Outline each blood parasite and name the species.
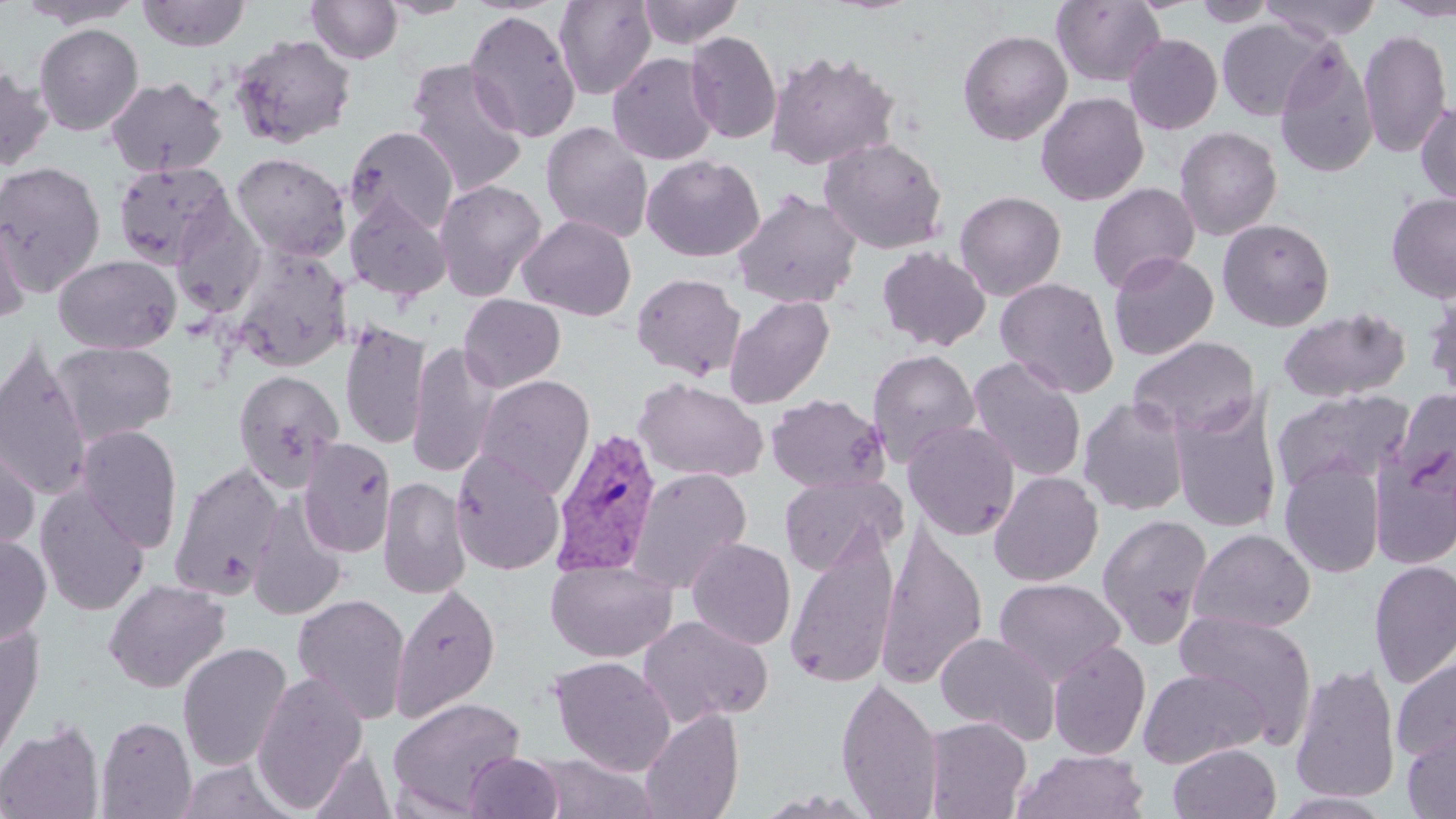
Approximate bounding boxes as named x1/y1/x2/y2 corners in pixels.
Plasmodium vivax-infected red blood cells: (x1=550, y1=426, x2=663, y2=578).
No Plasmodium falciparum, Plasmodium ovale, Plasmodium malariae, Babesia divergens, or Trypanosoma brucei observed.

slide-level diagnosis = Plasmodium vivax
modality = optical microscopy
field of view = single
stain = May-Grünwald-Giemsa
uninfected red blood cell locations = approximate bounding boxes as named x1/y1/x2/y2 corners in pixels: (x1=14, y1=0, x2=145, y2=28), (x1=136, y1=0, x2=251, y2=51), (x1=305, y1=0, x2=404, y2=65), (x1=378, y1=0, x2=476, y2=19), (x1=553, y1=0, x2=657, y2=100), (x1=636, y1=0, x2=744, y2=48), (x1=1051, y1=0, x2=1166, y2=87), (x1=1191, y1=0, x2=1279, y2=27), (x1=1259, y1=0, x2=1384, y2=43), (x1=1384, y1=0, x2=1456, y2=21), (x1=463, y1=9, x2=581, y2=143), (x1=1217, y1=18, x2=1329, y2=122), (x1=34, y1=23, x2=144, y2=135), (x1=1359, y1=28, x2=1451, y2=159), (x1=957, y1=29, x2=1072, y2=145), (x1=685, y1=30, x2=782, y2=144), (x1=1123, y1=33, x2=1223, y2=134), (x1=229, y1=34, x2=357, y2=149), (x1=1274, y1=41, x2=1378, y2=180), (x1=765, y1=49, x2=900, y2=170), (x1=606, y1=52, x2=719, y2=165), (x1=405, y1=59, x2=528, y2=197), (x1=0, y1=64, x2=55, y2=171), (x1=105, y1=76, x2=227, y2=177), (x1=1035, y1=91, x2=1149, y2=206), (x1=1416, y1=97, x2=1456, y2=205), (x1=541, y1=122, x2=654, y2=244), (x1=344, y1=126, x2=459, y2=235), (x1=1174, y1=126, x2=1282, y2=241), (x1=819, y1=136, x2=949, y2=254), (x1=231, y1=151, x2=351, y2=261), (x1=641, y1=154, x2=765, y2=262), (x1=0, y1=161, x2=106, y2=294), (x1=112, y1=161, x2=235, y2=269), (x1=433, y1=178, x2=548, y2=300), (x1=1087, y1=182, x2=1200, y2=293), (x1=732, y1=189, x2=862, y2=309), (x1=954, y1=190, x2=1067, y2=300), (x1=1386, y1=190, x2=1456, y2=303), (x1=344, y1=194, x2=453, y2=300), (x1=170, y1=207, x2=265, y2=316), (x1=0, y1=210, x2=30, y2=325), (x1=517, y1=214, x2=637, y2=321), (x1=1217, y1=218, x2=1336, y2=331), (x1=228, y1=245, x2=352, y2=372), (x1=876, y1=245, x2=991, y2=351), (x1=1108, y1=251, x2=1219, y2=360), (x1=53, y1=254, x2=181, y2=354), (x1=630, y1=272, x2=746, y2=380), (x1=995, y1=277, x2=1119, y2=397), (x1=1422, y1=289, x2=1456, y2=402), (x1=458, y1=294, x2=566, y2=391), (x1=724, y1=295, x2=835, y2=409), (x1=1276, y1=306, x2=1411, y2=403), (x1=339, y1=319, x2=430, y2=451), (x1=1128, y1=336, x2=1260, y2=438), (x1=407, y1=340, x2=500, y2=479), (x1=0, y1=341, x2=93, y2=502), (x1=50, y1=341, x2=178, y2=444), (x1=866, y1=348, x2=980, y2=466), (x1=967, y1=356, x2=1087, y2=483), (x1=232, y1=369, x2=344, y2=490), (x1=474, y1=374, x2=595, y2=497), (x1=633, y1=377, x2=767, y2=483), (x1=1393, y1=387, x2=1456, y2=487), (x1=1271, y1=389, x2=1415, y2=494), (x1=766, y1=393, x2=888, y2=493), (x1=1169, y1=394, x2=1283, y2=533), (x1=1078, y1=396, x2=1192, y2=517), (x1=902, y1=420, x2=1020, y2=540), (x1=77, y1=425, x2=183, y2=553), (x1=0, y1=435, x2=40, y2=557), (x1=298, y1=437, x2=396, y2=558), (x1=1370, y1=447, x2=1456, y2=569), (x1=450, y1=450, x2=566, y2=575), (x1=1279, y1=460, x2=1385, y2=578), (x1=170, y1=461, x2=284, y2=599), (x1=628, y1=467, x2=753, y2=593), (x1=989, y1=471, x2=1103, y2=586), (x1=778, y1=474, x2=904, y2=576), (x1=379, y1=476, x2=471, y2=600), (x1=35, y1=483, x2=151, y2=617), (x1=247, y1=497, x2=347, y2=621), (x1=1097, y1=513, x2=1213, y2=648), (x1=874, y1=525, x2=988, y2=691), (x1=1188, y1=527, x2=1316, y2=634), (x1=785, y1=528, x2=900, y2=690), (x1=0, y1=533, x2=52, y2=645), (x1=686, y1=537, x2=796, y2=650), (x1=545, y1=558, x2=677, y2=663), (x1=1368, y1=559, x2=1456, y2=689), (x1=994, y1=577, x2=1125, y2=686), (x1=103, y1=578, x2=230, y2=693), (x1=390, y1=583, x2=501, y2=722), (x1=292, y1=592, x2=411, y2=724), (x1=1173, y1=609, x2=1317, y2=743), (x1=637, y1=615, x2=773, y2=726), (x1=0, y1=623, x2=43, y2=770), (x1=935, y1=631, x2=1061, y2=743), (x1=1048, y1=639, x2=1151, y2=760), (x1=177, y1=641, x2=293, y2=773), (x1=1392, y1=655, x2=1456, y2=765), (x1=548, y1=656, x2=676, y2=775), (x1=1289, y1=660, x2=1401, y2=804), (x1=1137, y1=667, x2=1268, y2=768), (x1=251, y1=670, x2=369, y2=812), (x1=836, y1=675, x2=944, y2=818), (x1=387, y1=696, x2=526, y2=815), (x1=640, y1=708, x2=744, y2=819), (x1=96, y1=715, x2=196, y2=818), (x1=924, y1=716, x2=1031, y2=819), (x1=0, y1=720, x2=105, y2=819), (x1=1402, y1=726, x2=1456, y2=818), (x1=1168, y1=742, x2=1281, y2=819), (x1=307, y1=747, x2=396, y2=819), (x1=1013, y1=749, x2=1150, y2=819), (x1=462, y1=752, x2=564, y2=818), (x1=175, y1=758, x2=299, y2=819), (x1=1273, y1=791, x2=1396, y2=817)
preparation = thin blood film
magnification = 1000x
image size = 1456×819 pixels